Report the malaria status.
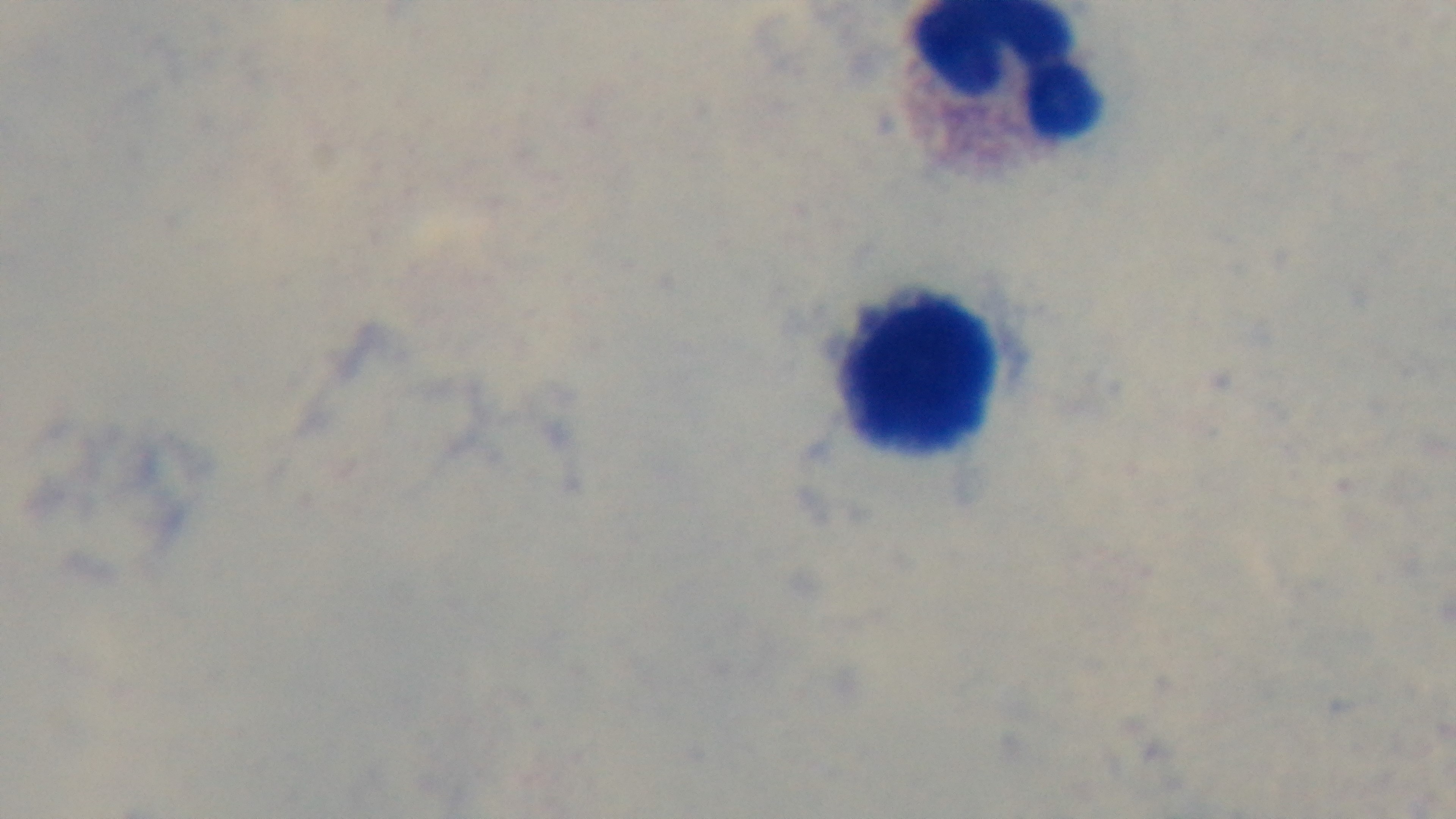
Uninfected.

Giemsa-stained. 100x oil-immersion objective. Preparation: thick. Captured with a mounted 4K digital camera. Photomicrograph. One field from the slide.